Report the malaria status of this cell.
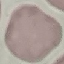

It is uninfected.

Summary:
  - Stain: Giemsa
  - Preparation: thin blood film
  - Image type: automatically extracted cell patch, resized to 64 × 64 pixels
  - Capture: smartphone through the microscope eyepiece